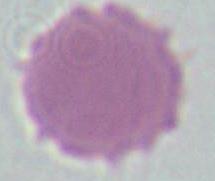
magnification = 1000x
identification = erythrocyte
modality = photomicrograph